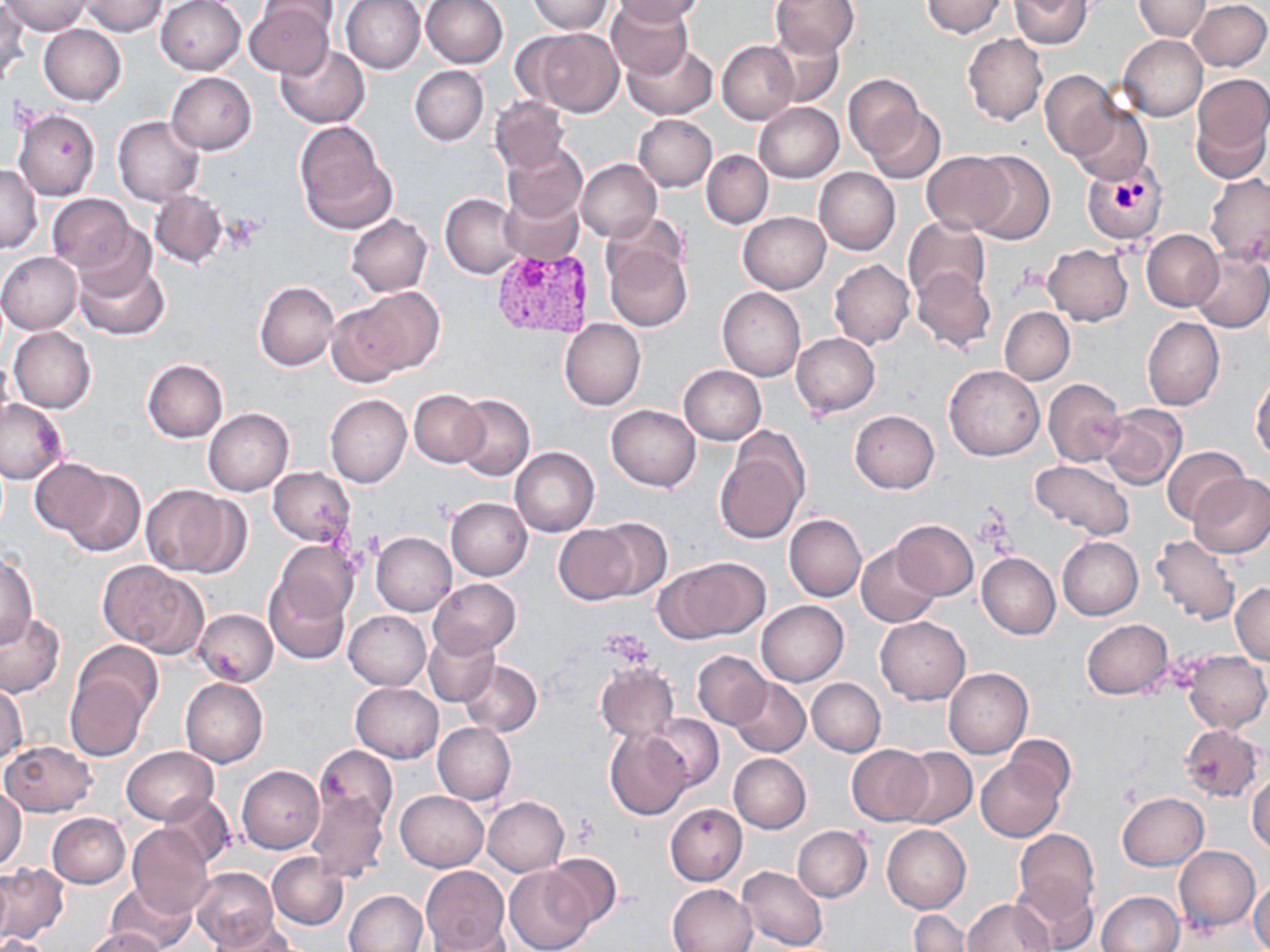

Summary:
  - Coordinate format: approximate bounding boxes as [x1, y1, x2, y2] in pixels
  - Platelet locations: [1016, 262, 1052, 292], [975, 508, 1014, 553]
  - Uninfected red blood cell locations: [4, 0, 89, 34], [342, 0, 426, 73], [420, 0, 507, 69], [528, 0, 613, 34], [612, 0, 707, 25], [771, 0, 861, 58], [921, 0, 1008, 37], [1134, 0, 1210, 40], [1188, 0, 1269, 72], [80, 1, 169, 36], [155, 1, 246, 75], [257, 1, 340, 32], [607, 1, 693, 79], [1010, 1, 1092, 49], [244, 3, 335, 79], [0, 4, 27, 82], [39, 24, 126, 104], [520, 27, 624, 117], [766, 29, 843, 106], [963, 33, 1047, 125], [1119, 35, 1207, 120], [623, 41, 718, 120], [718, 41, 797, 124], [274, 44, 370, 128], [410, 66, 488, 146], [1040, 70, 1119, 160], [166, 72, 256, 154], [1190, 73, 1270, 180], [843, 74, 926, 160], [489, 95, 569, 173], [753, 103, 843, 183], [1072, 106, 1152, 185], [865, 108, 945, 183], [14, 109, 101, 200], [633, 114, 717, 190], [113, 116, 204, 206], [294, 122, 395, 233], [502, 142, 588, 223], [702, 149, 773, 228], [922, 151, 1014, 234], [967, 151, 1056, 244], [576, 158, 661, 242], [0, 163, 42, 254], [815, 168, 901, 254], [1204, 174, 1270, 267], [498, 188, 584, 266], [149, 190, 227, 267], [441, 193, 524, 278], [46, 194, 136, 274], [599, 212, 689, 292], [738, 212, 830, 293], [345, 214, 433, 296], [903, 217, 990, 304], [1142, 229, 1223, 311], [605, 239, 692, 332], [1043, 245, 1133, 326], [73, 249, 170, 342], [1191, 250, 1270, 332], [0, 251, 83, 333], [830, 259, 914, 349], [912, 268, 996, 353], [254, 281, 339, 371], [348, 288, 445, 376], [717, 288, 806, 381], [325, 302, 413, 389], [1000, 306, 1074, 383], [1143, 316, 1224, 411], [559, 319, 646, 410], [9, 327, 96, 413], [791, 333, 880, 417], [142, 359, 228, 442], [678, 365, 768, 445], [944, 365, 1044, 461], [1251, 377, 1270, 460], [1044, 378, 1126, 467], [409, 390, 488, 467], [325, 395, 412, 488], [453, 395, 534, 481], [0, 399, 68, 485], [607, 405, 701, 491], [1099, 405, 1185, 491], [204, 408, 294, 495], [849, 410, 940, 493], [715, 435, 809, 544], [1163, 446, 1252, 526], [510, 447, 599, 536], [29, 458, 113, 538], [1029, 459, 1134, 541], [269, 467, 357, 547], [59, 468, 146, 557], [1189, 472, 1270, 558], [144, 485, 244, 577], [445, 498, 532, 580], [785, 514, 866, 602], [587, 518, 672, 600], [891, 520, 978, 600], [553, 525, 640, 605], [372, 532, 456, 616], [1150, 534, 1241, 627], [1058, 536, 1143, 619], [272, 540, 360, 626], [857, 544, 941, 627], [0, 552, 39, 647], [977, 553, 1060, 639], [660, 558, 769, 642], [98, 561, 205, 654], [265, 574, 350, 663], [429, 579, 520, 656], [1230, 583, 1270, 665], [756, 599, 848, 686], [195, 609, 278, 686], [343, 611, 430, 690], [0, 612, 68, 698], [876, 617, 969, 704], [1081, 619, 1175, 700], [423, 630, 500, 707], [73, 640, 164, 720], [693, 650, 770, 729], [1184, 650, 1269, 733], [460, 660, 543, 737], [596, 663, 679, 742], [944, 667, 1033, 757], [65, 671, 149, 762], [807, 677, 886, 757], [730, 678, 811, 756], [181, 679, 268, 767], [351, 683, 444, 763], [1, 684, 28, 764], [644, 713, 724, 791], [433, 723, 515, 805], [1180, 723, 1264, 801], [605, 728, 692, 820], [1006, 735, 1075, 804], [1, 740, 96, 817], [846, 744, 934, 826], [314, 745, 399, 830], [121, 746, 217, 824], [895, 747, 976, 829], [728, 753, 810, 833], [975, 757, 1066, 842], [237, 765, 325, 853], [1248, 773, 1270, 853], [0, 785, 27, 870], [395, 790, 488, 871], [307, 791, 389, 884], [1117, 792, 1209, 870], [157, 793, 234, 869], [483, 797, 569, 877], [665, 803, 747, 885], [47, 812, 131, 888], [127, 824, 214, 917], [792, 824, 872, 901], [882, 824, 971, 912], [1015, 829, 1099, 916], [1174, 846, 1259, 931], [541, 852, 622, 930], [266, 853, 349, 930], [0, 863, 68, 943], [736, 865, 828, 951], [420, 866, 510, 952], [0, 867, 13, 944], [190, 867, 279, 950], [506, 869, 591, 951], [1011, 870, 1100, 952], [1249, 878, 1270, 952], [106, 881, 195, 952], [667, 883, 757, 952], [344, 890, 428, 952], [1097, 892, 1182, 952], [962, 899, 1054, 951], [909, 910, 969, 952], [210, 917, 295, 952], [82, 927, 168, 952], [420, 928, 516, 952], [0, 935, 47, 951]
  - Plasmodium vivax-infected red blood cell locations: [1081, 156, 1169, 244], [490, 247, 597, 342]
  - Slide-level diagnosis: Plasmodium vivax
  - Stain: May-Grünwald-Giemsa
  - Magnification: 1000x
  - Image size: 1270×952 pixels
  - Field of view: one of a larger specimen
  - Preparation: thin blood film
  - Modality: optical microscopy